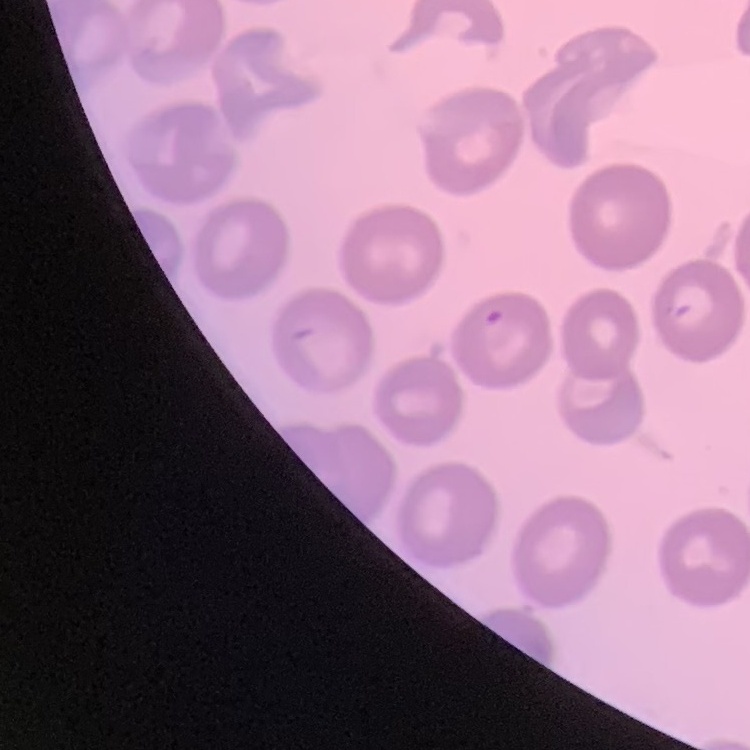

{
  "red_blood_cell_morphology": "no rouleaux formation",
  "preparation": "thin peripheral smear",
  "image_type": "one tile cut from a larger photomicrograph",
  "stain": "Field's or Giemsa"
}